Mark where platelets are.
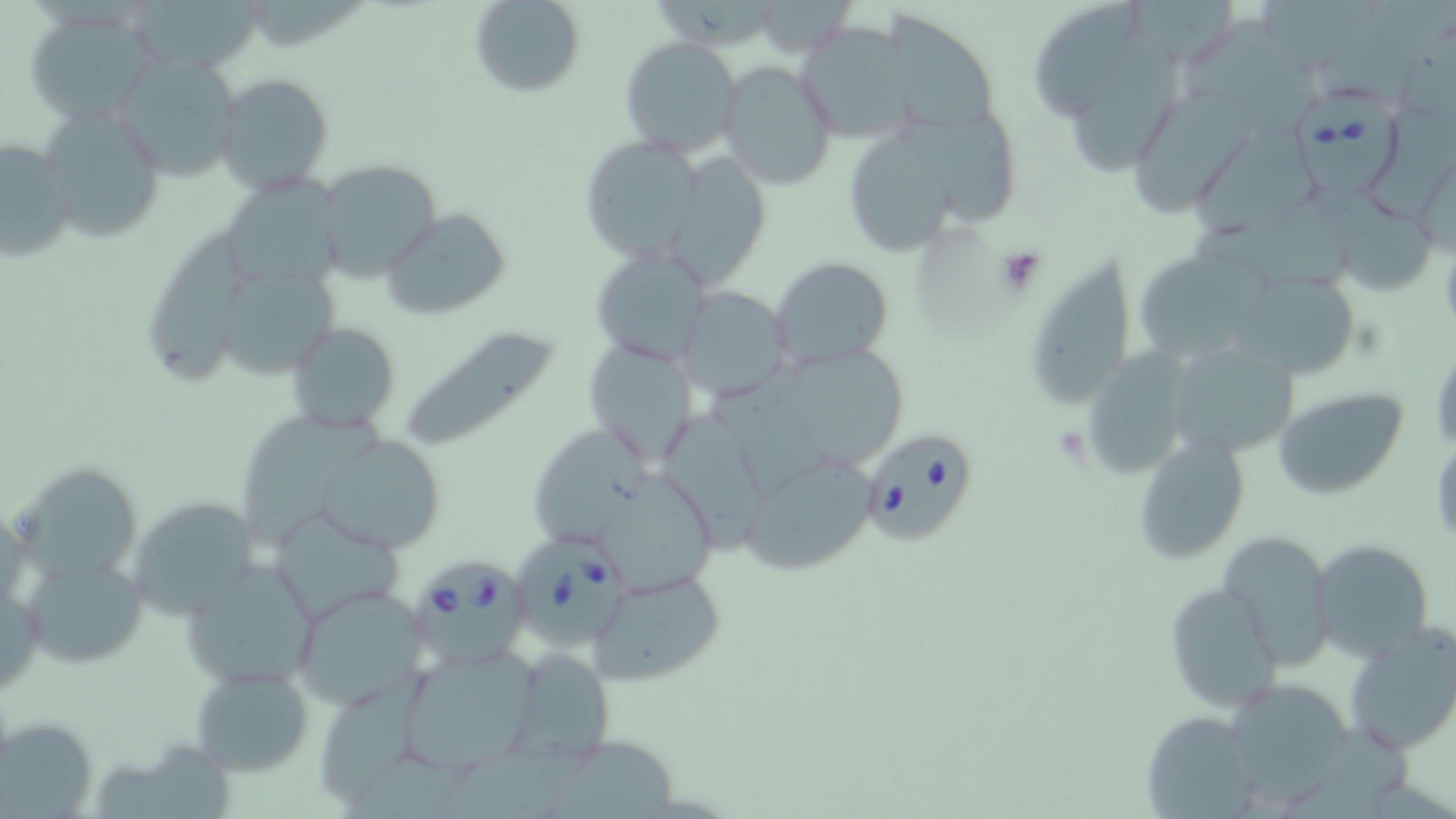

Approximate bounding boxes as [x1, y1, x2, y2] in pixels.
Platelets: [993, 245, 1048, 295].

{
  "slide_level_diagnosis": "Babesia divergens",
  "stain": "May-Grünwald-Giemsa",
  "uninfected_red_blood_cell_locations": "approximate bounding boxes as [x1, y1, x2, y2] in pixels: [130, 0, 266, 75], [467, 0, 585, 97], [1032, 0, 1144, 123], [1122, 0, 1235, 59], [1258, 0, 1378, 63], [21, 7, 158, 121], [1181, 18, 1318, 135], [794, 21, 919, 147], [619, 37, 740, 156], [113, 53, 242, 180], [898, 56, 997, 138], [1077, 57, 1184, 175], [717, 62, 835, 191], [213, 71, 333, 193], [1135, 86, 1255, 220], [1372, 101, 1456, 225], [39, 104, 166, 242], [901, 118, 1018, 227], [1197, 126, 1316, 242], [849, 135, 953, 257], [0, 137, 77, 264], [576, 137, 702, 265], [1414, 148, 1456, 262], [667, 155, 776, 287], [311, 160, 446, 281], [225, 174, 351, 292], [1331, 196, 1440, 298], [1189, 207, 1354, 296], [380, 208, 512, 318], [144, 225, 252, 394], [591, 248, 713, 367], [1035, 250, 1131, 403], [768, 256, 893, 369], [1138, 256, 1271, 364], [222, 273, 340, 375], [1238, 279, 1353, 378], [677, 287, 791, 400], [397, 321, 566, 454], [287, 323, 400, 434], [583, 335, 702, 468], [1163, 340, 1299, 459], [1094, 342, 1179, 479], [1429, 343, 1456, 458], [785, 346, 902, 465], [712, 359, 832, 501], [1271, 387, 1407, 498], [239, 412, 388, 549], [659, 413, 766, 556], [535, 431, 646, 541], [322, 434, 443, 553], [1131, 437, 1249, 564], [740, 452, 881, 575], [15, 462, 151, 588], [600, 481, 715, 602], [126, 494, 261, 618], [271, 515, 410, 620], [1218, 529, 1337, 668], [1310, 539, 1433, 662], [27, 556, 155, 674], [180, 559, 317, 689], [588, 568, 727, 686], [1163, 580, 1283, 713], [290, 584, 430, 710], [1342, 624, 1456, 757], [396, 647, 540, 772], [502, 648, 615, 765], [188, 663, 315, 778], [313, 684, 424, 809], [1235, 685, 1349, 804], [1140, 709, 1260, 816], [1, 715, 101, 819], [1281, 725, 1417, 819], [540, 740, 677, 819], [91, 741, 228, 819], [438, 745, 579, 819], [338, 754, 473, 819]",
  "field_of_view": "single",
  "image_size": "1456×819 pixels",
  "preparation": "thin blood smear",
  "babesia_divergens_infected_red_blood_cell_locations": "approximate bounding boxes as [x1, y1, x2, y2] in pixels: [1292, 83, 1403, 202], [855, 427, 980, 547], [518, 532, 629, 642], [415, 559, 531, 666]",
  "modality": "optical microscopy",
  "magnification": "1000x"
}